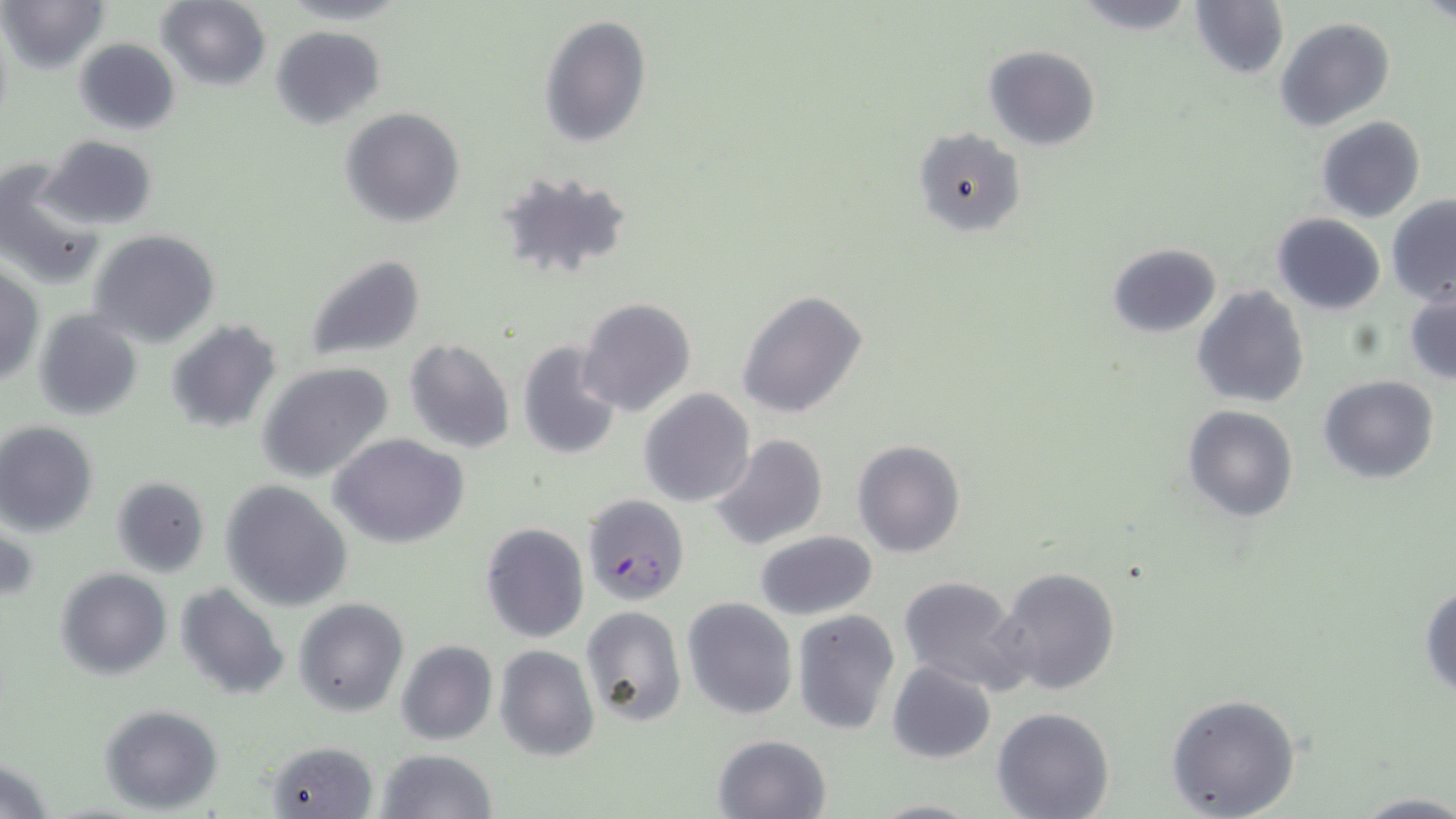

Approximate bounding boxes as named x1/y1/x2/y2 corners in pixels. Uninfected red blood cell locations: (x1=3, y1=0, x2=110, y2=73), (x1=278, y1=0, x2=410, y2=25), (x1=1069, y1=0, x2=1198, y2=35), (x1=1189, y1=0, x2=1290, y2=80), (x1=156, y1=1, x2=271, y2=89), (x1=539, y1=15, x2=651, y2=147), (x1=1274, y1=16, x2=1396, y2=131), (x1=271, y1=25, x2=384, y2=130), (x1=72, y1=38, x2=180, y2=135), (x1=983, y1=44, x2=1100, y2=151), (x1=340, y1=107, x2=466, y2=229), (x1=1315, y1=116, x2=1425, y2=222), (x1=913, y1=127, x2=1026, y2=238), (x1=42, y1=135, x2=158, y2=231), (x1=0, y1=161, x2=108, y2=290), (x1=500, y1=170, x2=634, y2=283), (x1=1387, y1=196, x2=1456, y2=305), (x1=1270, y1=213, x2=1385, y2=315), (x1=87, y1=228, x2=221, y2=348), (x1=1107, y1=243, x2=1222, y2=338), (x1=302, y1=252, x2=427, y2=361), (x1=0, y1=267, x2=44, y2=385), (x1=1191, y1=285, x2=1310, y2=410), (x1=1405, y1=288, x2=1456, y2=385), (x1=735, y1=289, x2=869, y2=420), (x1=577, y1=297, x2=696, y2=417), (x1=33, y1=310, x2=142, y2=421), (x1=165, y1=319, x2=282, y2=436), (x1=404, y1=338, x2=515, y2=455), (x1=515, y1=341, x2=621, y2=461), (x1=257, y1=362, x2=395, y2=485), (x1=1319, y1=375, x2=1439, y2=483), (x1=639, y1=389, x2=756, y2=509), (x1=1183, y1=405, x2=1297, y2=523), (x1=0, y1=422, x2=99, y2=536), (x1=330, y1=433, x2=470, y2=549), (x1=709, y1=435, x2=829, y2=552), (x1=851, y1=438, x2=966, y2=558), (x1=109, y1=476, x2=211, y2=578), (x1=220, y1=480, x2=353, y2=611), (x1=479, y1=521, x2=590, y2=643), (x1=754, y1=530, x2=877, y2=621), (x1=996, y1=565, x2=1121, y2=696), (x1=56, y1=568, x2=171, y2=680), (x1=896, y1=575, x2=1029, y2=694), (x1=1420, y1=581, x2=1456, y2=699), (x1=177, y1=583, x2=286, y2=700), (x1=787, y1=594, x2=993, y2=717), (x1=682, y1=597, x2=796, y2=719), (x1=295, y1=598, x2=408, y2=717), (x1=581, y1=606, x2=686, y2=726), (x1=792, y1=609, x2=899, y2=734), (x1=396, y1=640, x2=497, y2=745), (x1=493, y1=645, x2=600, y2=760), (x1=886, y1=660, x2=997, y2=764), (x1=1166, y1=693, x2=1301, y2=817), (x1=99, y1=704, x2=224, y2=813), (x1=992, y1=707, x2=1115, y2=819), (x1=712, y1=733, x2=834, y2=819), (x1=263, y1=738, x2=381, y2=819), (x1=375, y1=749, x2=497, y2=819), (x1=0, y1=760, x2=56, y2=816), (x1=1354, y1=793, x2=1456, y2=817), (x1=864, y1=797, x2=983, y2=818). Plasmodium falciparum-infected red blood cell locations: (x1=585, y1=494, x2=688, y2=605). Slide-level diagnosis: Plasmodium falciparum. Image is 1456×819 pixels. Captured at 1000x magnification. Thin blood smear. Optical microscopy. One field of a larger specimen. May-Grünwald-Giemsa stain.